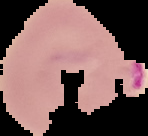
Malaria status: parasitized. Cell region segmented out of the field of view; the surrounding area is masked to black. Image is 148×136 pixels. From a thin blood smear.